Locate every malaria parasite.
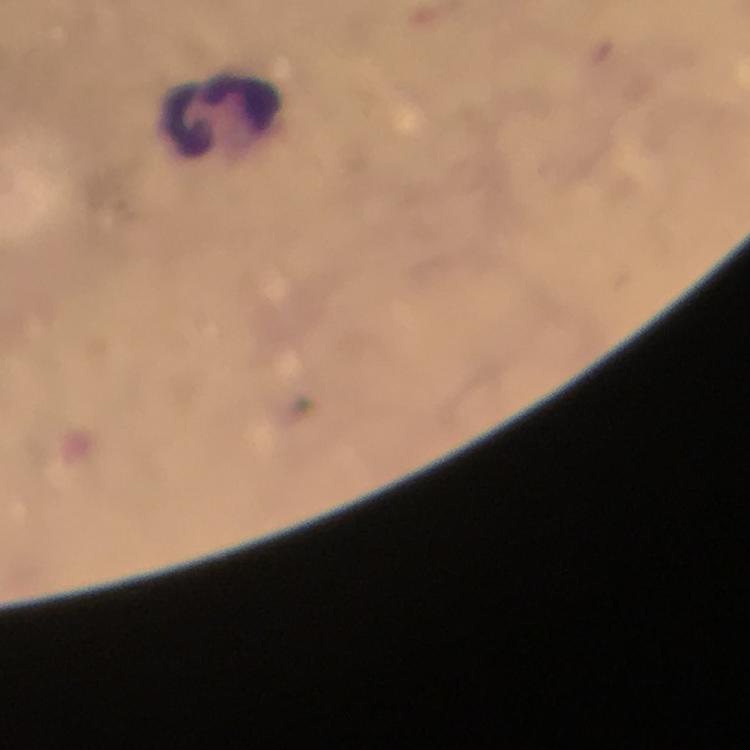
No malaria parasites seen.

Approximate centers as [x, y] in pixels. Leukocyte locations: [220, 113]. Thick smear. Immersion oil was used. Giemsa stain. A crop from one field of view. From a diagnostic examination for malaria. At 100x magnification. Photographed through the microscope with a smartphone camera. Image is 750×750 pixels.